Locate every blood parasite and identify its species.
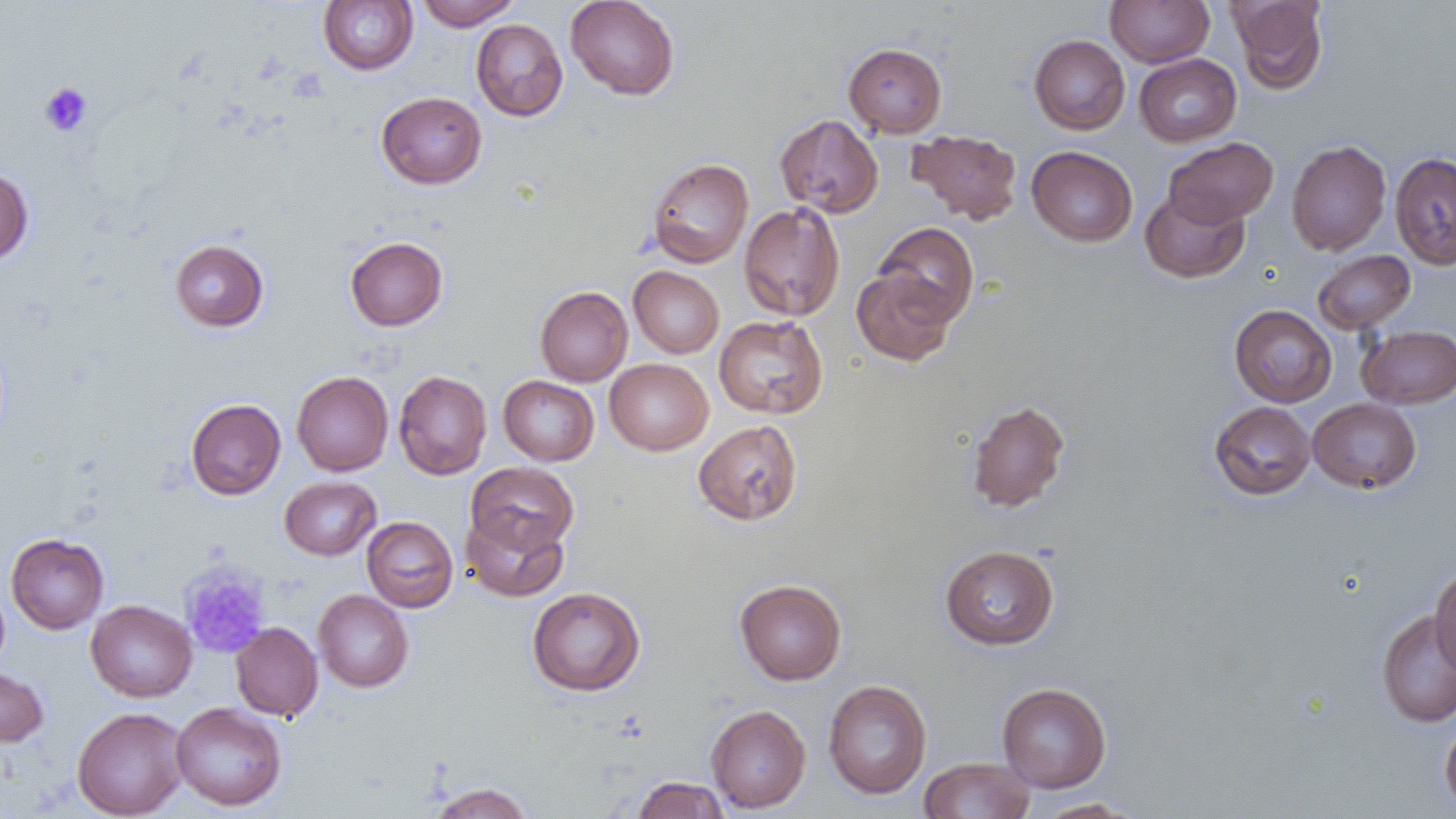
No blood parasites observed.

Approximate bounding boxes as (x1, y1, x2, y2) in pixels. Uninfected red blood cell locations: (416, 0, 521, 30), (565, 0, 680, 100), (1105, 0, 1215, 67), (1229, 0, 1327, 92), (318, 1, 418, 74), (471, 19, 567, 121), (1029, 34, 1130, 134), (844, 43, 947, 137), (1134, 54, 1241, 147), (376, 91, 487, 189), (775, 114, 884, 218), (908, 130, 1022, 224), (1164, 137, 1277, 228), (1286, 140, 1391, 256), (1027, 146, 1137, 246), (1390, 152, 1456, 270), (647, 157, 754, 268), (0, 166, 34, 265), (1140, 188, 1249, 283), (739, 202, 845, 321), (873, 222, 979, 327), (345, 236, 447, 331), (169, 238, 269, 332), (1312, 250, 1416, 334), (628, 266, 724, 358), (852, 269, 956, 366), (535, 286, 633, 386), (1229, 304, 1337, 407), (714, 315, 828, 419), (1356, 325, 1456, 409), (604, 358, 713, 455), (393, 370, 492, 480), (292, 371, 393, 476), (499, 375, 599, 466), (186, 398, 286, 499), (966, 398, 1071, 513), (1308, 398, 1421, 493), (1209, 401, 1316, 500), (693, 419, 803, 525), (465, 462, 579, 556), (280, 476, 380, 560), (461, 511, 569, 602), (362, 516, 458, 613), (5, 532, 109, 634), (940, 544, 1059, 650), (1430, 567, 1456, 674), (735, 578, 847, 685), (527, 586, 646, 696), (313, 589, 414, 692), (86, 599, 197, 702), (1376, 609, 1455, 727), (231, 622, 322, 721), (0, 664, 49, 747), (823, 680, 932, 799), (997, 682, 1111, 792), (171, 702, 287, 810), (705, 704, 811, 813), (72, 706, 189, 818), (1440, 720, 1456, 812), (918, 757, 1034, 819), (631, 776, 731, 818), (427, 782, 534, 819), (1034, 798, 1143, 818). Platelet locations: (39, 82, 93, 136), (179, 566, 270, 658). Slide-level diagnosis: no evidence of blood parasites. Thin blood smear. Image is 1456×819 pixels. Single field of view. Light microscopy. Captured at 1000x magnification.